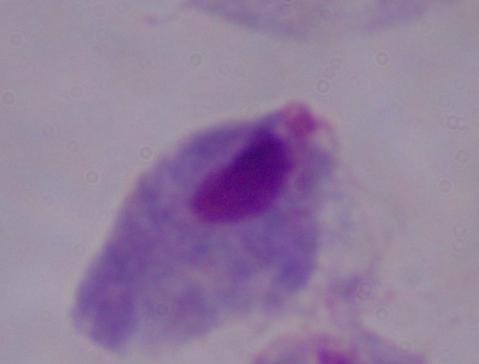
Captured at 1000x magnification. A trichomonad is shown. Photomicrograph.